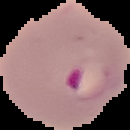

Summary:
  - Image type: cell region segmented out of the field of view; surrounding area masked to black
  - Malaria status: parasitized
  - Preparation: thin blood smear
  - Image size: 130×130 pixels